Assess this cell for malaria.
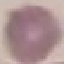

It is uninfected.

Thin blood film. Giemsa stain. Automatically extracted cell patch, resized to 64 × 64 pixels. Photographed with a smartphone camera at the microscope eyepiece.